Locate Plasmodium parasites and leukocytes.
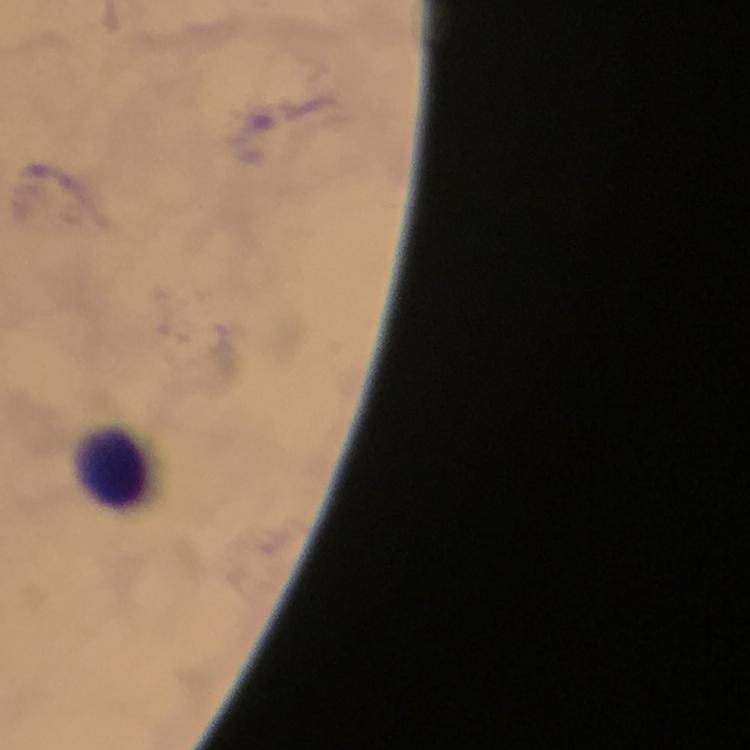

No Plasmodium parasites seen.
Approximate centers as (x, y) in pixels.
Leukocytes: (114, 468).

{
  "immersion_oil": "applied",
  "context": "from a malaria diagnostic workup",
  "preparation": "thick smear",
  "stain": "Giemsa",
  "magnification": "100x",
  "image_size": "750×750 pixels",
  "capture": "smartphone photograph through a microscope",
  "cropped_from": "one field of view"
}